Outline each blood parasite and name the species.
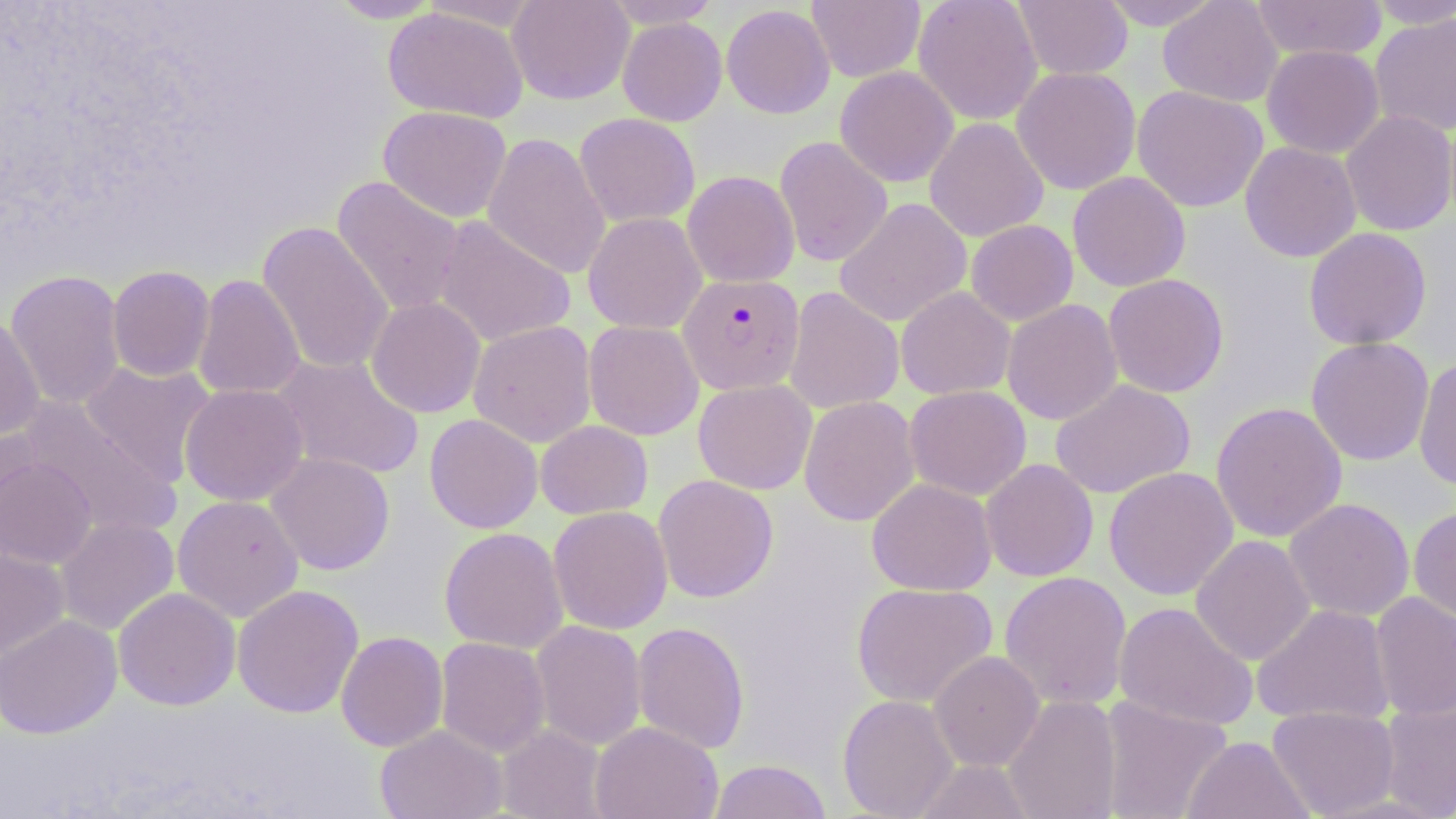
Approximate bounding boxes as (x1, y1, x2, y2) in pixels.
Plasmodium falciparum-infected red blood cells: (678, 273, 805, 395).
No Plasmodium ovale, Plasmodium malariae, Plasmodium vivax, Babesia divergens, or Trypanosoma brucei observed.

Uninfected red blood cell locations: (325, 0, 445, 23), (507, 0, 635, 105), (602, 0, 722, 28), (807, 0, 925, 83), (913, 0, 1043, 125), (1012, 0, 1133, 80), (1097, 0, 1227, 30), (1157, 0, 1283, 107), (1249, 0, 1388, 62), (1364, 0, 1456, 29), (721, 3, 835, 119), (383, 6, 528, 123), (1369, 13, 1456, 138), (617, 17, 727, 126), (1261, 44, 1384, 159), (1011, 65, 1141, 195), (834, 66, 959, 187), (1131, 85, 1268, 213), (378, 106, 512, 223), (1340, 110, 1456, 236), (574, 112, 700, 227), (924, 117, 1049, 242), (482, 132, 611, 280), (774, 136, 893, 267), (1240, 141, 1361, 262), (682, 171, 800, 288), (1067, 171, 1190, 292), (330, 176, 466, 318), (834, 197, 972, 327), (583, 212, 707, 334), (432, 215, 576, 348), (966, 219, 1078, 326), (257, 220, 395, 376), (1304, 227, 1432, 350), (107, 265, 215, 382), (5, 269, 125, 410), (1103, 273, 1229, 398), (192, 274, 306, 401), (783, 286, 905, 415), (896, 286, 1015, 401), (366, 297, 486, 418), (1002, 299, 1123, 425), (0, 314, 44, 440), (468, 320, 597, 447), (583, 320, 704, 440), (1306, 336, 1434, 466), (270, 352, 424, 481), (1413, 357, 1456, 491), (80, 360, 216, 486), (693, 379, 817, 495), (1050, 379, 1195, 499), (179, 383, 309, 506), (904, 385, 1031, 501), (798, 395, 920, 526), (19, 399, 180, 538), (1210, 401, 1347, 542), (424, 414, 543, 534), (535, 420, 653, 520), (1, 424, 42, 531), (266, 452, 395, 575), (0, 457, 97, 569), (980, 459, 1098, 583), (1104, 466, 1238, 600), (653, 474, 779, 603), (866, 477, 996, 596), (172, 494, 304, 621), (1284, 498, 1415, 621), (548, 505, 673, 634), (1408, 505, 1456, 627), (55, 516, 179, 635), (439, 527, 568, 653), (1190, 535, 1316, 665), (0, 546, 69, 659), (999, 570, 1132, 711), (851, 582, 998, 708), (232, 585, 363, 718), (113, 587, 240, 710), (1370, 592, 1456, 721), (1114, 601, 1259, 732), (1251, 603, 1395, 728), (0, 614, 122, 739), (531, 620, 647, 750), (632, 622, 750, 755), (335, 631, 448, 752), (435, 637, 551, 757), (929, 651, 1045, 771), (837, 694, 959, 819), (1003, 694, 1122, 819), (1098, 696, 1233, 819), (1378, 697, 1456, 818), (1267, 706, 1400, 817), (590, 722, 723, 819), (375, 725, 507, 819), (495, 725, 608, 819), (1182, 735, 1315, 819), (913, 758, 1033, 818), (708, 759, 832, 819). Slide-level diagnosis: Plasmodium falciparum. Single field of view. Thin blood smear. Captured at 1000x magnification. Image is 1456×819 pixels. May-Grünwald-Giemsa stain. Light microscopy.